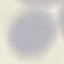 Malaria status: uninfected. Giemsa stain. Thin smear of blood. Cell patch, automatically extracted from a larger field of view and resized to 64 × 64 pixels. Acquired by smartphone through the microscope eyepiece.